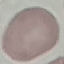
result = negative for malaria parasites
capture = smartphone camera at the microscope eyepiece
image type = cell patch, automatically extracted from a larger field of view and resized to 64 × 64 pixels
stain = Giemsa
preparation = thin smear